Report the malaria status.
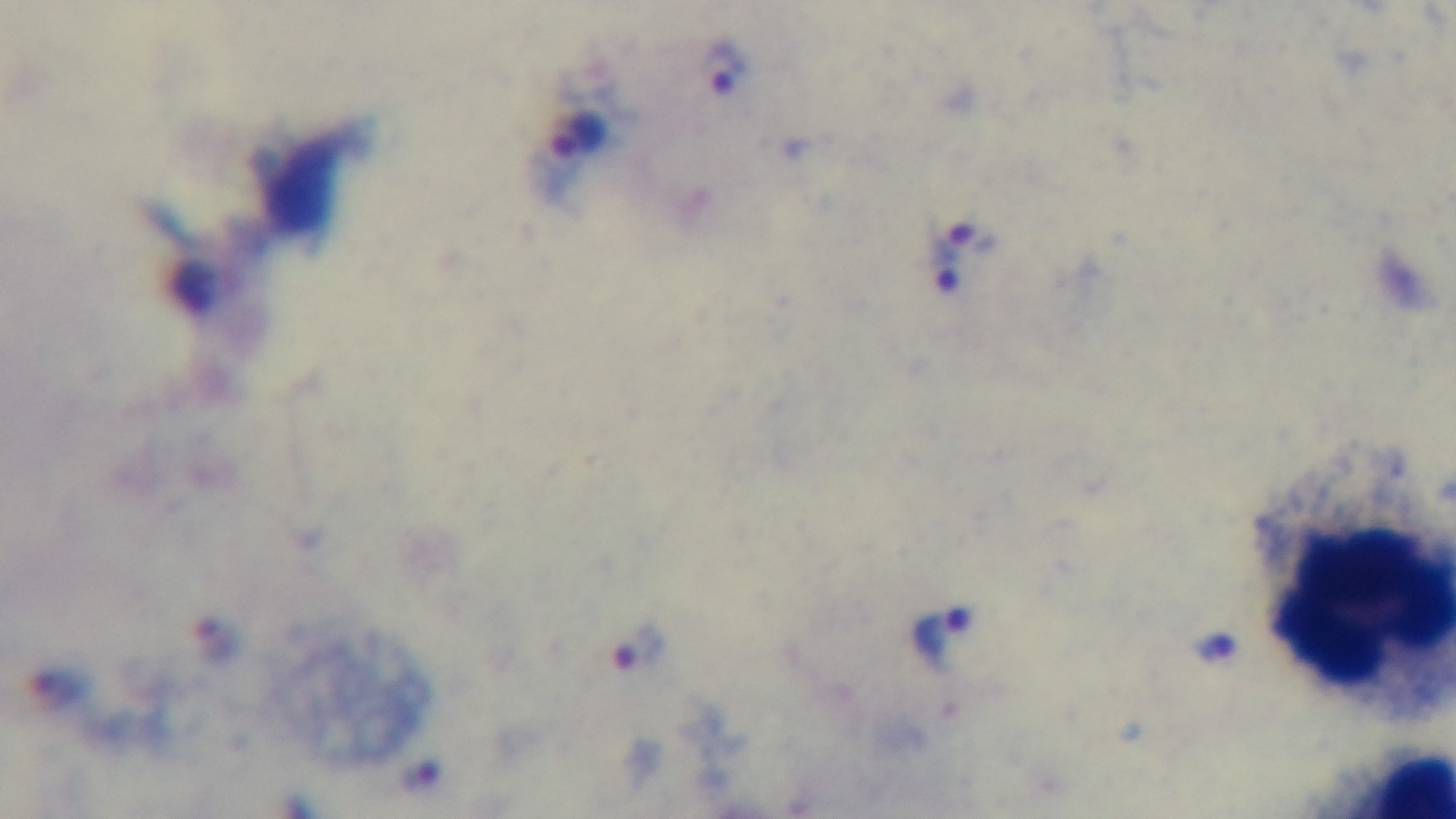
Positive.

field_of_view: one from the slide
capture: mounted 4K digital camera
modality: light microscopy
preparation: thick smear
stain: Giemsa
objective: 100x oil immersion